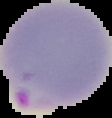

{
  "malaria_status": "parasitized",
  "preparation": "thin blood film",
  "image_type": "cell region segmented out of the field of view; surrounding area masked to black",
  "image_size": "112×118 pixels"
}